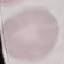

Result: negative for malaria parasites. Thin blood film. Giemsa stain. Photographed with a smartphone camera at the microscope eyepiece. Automatically extracted cell patch, resized to 64 × 64 pixels.